Identify the parasite.
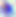

This is Toxoplasma gondii.

Summary:
  - Modality: micrograph
  - Magnification: 400x